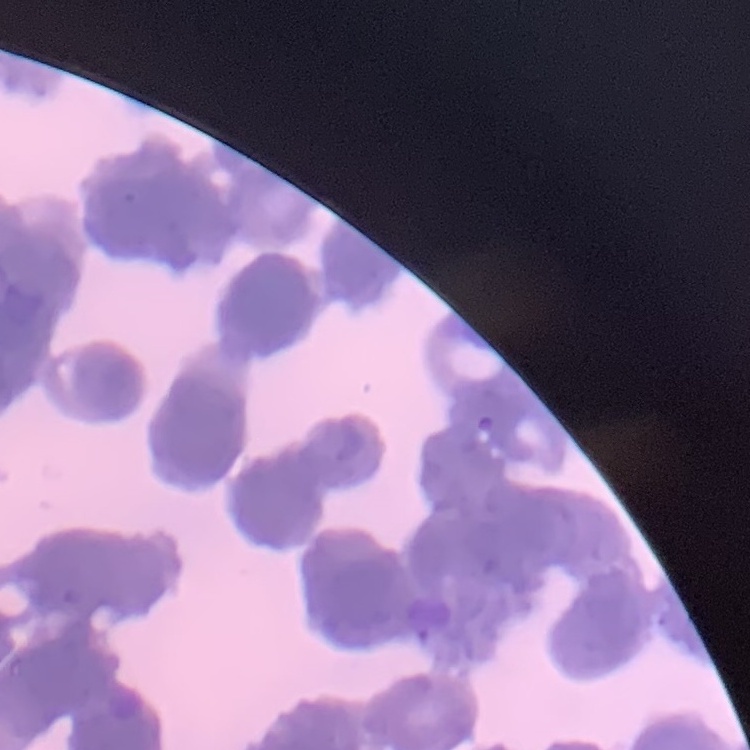
erythrocyte morphology = rouleaux formation
stain = Field's or Giemsa
preparation = thin peripheral smear
image type = square crop of a larger photomicrograph